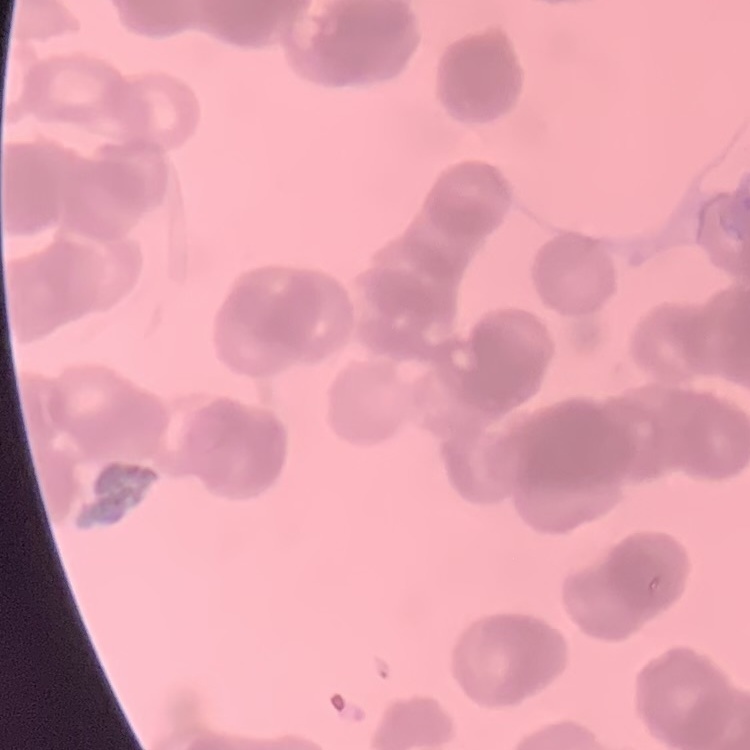

Summary:
  - Erythrocyte morphology: rouleaux formation
  - Stain: Field's or Giemsa
  - Preparation: thin blood film
  - Image type: square crop of a larger photomicrograph